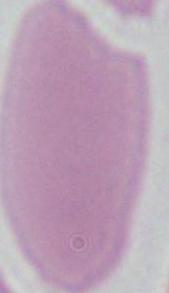 1000x magnification. A red blood cell is seen. Photomicrograph.